Classify this cell by malaria status.
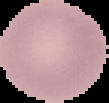
It is uninfected.

Summary:
  - Preparation: thin blood smear
  - Image type: cell region segmented out of the field of view; surrounding area masked to black
  - Image size: 109×103 pixels